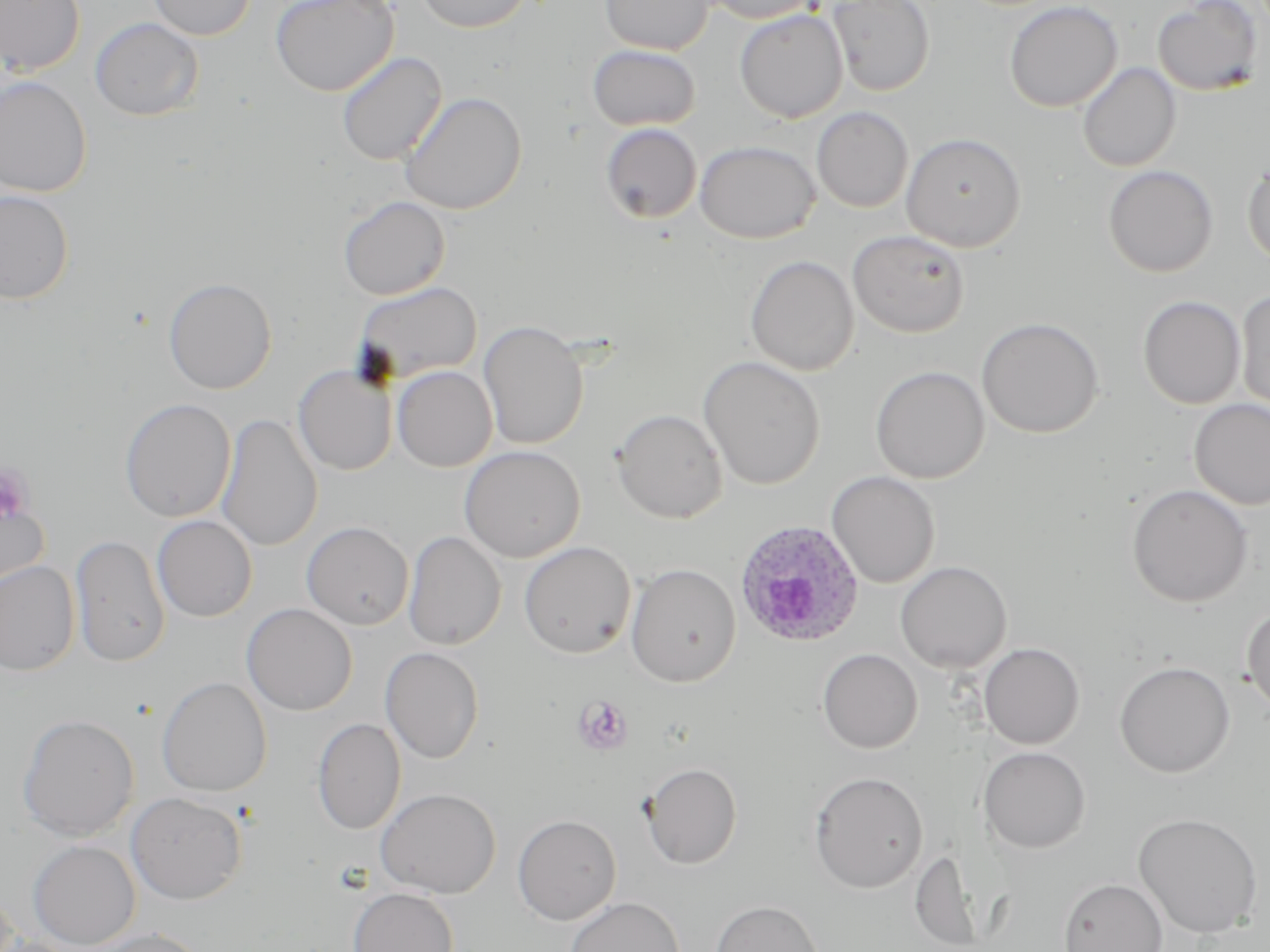

slide_level_diagnosis: Plasmodium ovale
magnification: 1000x
plasmodium_ovale_infected_red_blood_cell_locations: 'approximate bounding boxes as [x1, y1, x2, y2] in pixels: [735, 520, 864, 647]'
field_of_view: single
image_size: 1270×952 pixels
modality: optical microscopy
stain: May-Grünwald-Giemsa
preparation: thin blood film
platelet_locations: 'approximate bounding boxes as [x1, y1, x2, y2] in pixels: [0, 462, 35, 525], [573, 695, 634, 755]'
uninfected_red_blood_cell_locations: 'approximate bounding boxes as [x1, y1, x2, y2] in pixels: [0, 0, 85, 76], [147, 0, 255, 40], [270, 0, 399, 96], [415, 0, 533, 33], [599, 0, 713, 55], [697, 0, 822, 24], [827, 0, 935, 96], [1004, 0, 1123, 113], [1153, 0, 1264, 96], [734, 9, 848, 123], [90, 17, 204, 121], [587, 45, 701, 131], [337, 51, 447, 166], [1077, 62, 1181, 173], [0, 76, 92, 197], [400, 91, 526, 215], [812, 107, 914, 213], [600, 123, 702, 223], [901, 132, 1027, 252], [695, 140, 820, 243], [1243, 159, 1270, 267], [1103, 165, 1218, 277], [0, 190, 74, 305], [338, 196, 450, 300], [848, 230, 970, 338], [745, 255, 859, 376], [163, 277, 277, 394], [354, 282, 482, 384], [1235, 290, 1270, 415], [1138, 296, 1246, 409], [976, 317, 1104, 438], [479, 319, 589, 450], [698, 356, 825, 491], [293, 364, 397, 475], [392, 365, 497, 472], [871, 366, 989, 483], [119, 398, 236, 522], [1188, 398, 1270, 510], [611, 408, 728, 523], [215, 413, 323, 551], [460, 445, 585, 562], [826, 471, 941, 588], [1126, 484, 1254, 607], [0, 491, 50, 598], [152, 515, 257, 622], [301, 521, 414, 630], [403, 531, 506, 650], [70, 534, 170, 667], [519, 541, 636, 658], [0, 561, 81, 676], [894, 561, 1012, 673], [626, 563, 741, 687], [241, 603, 358, 715], [1242, 605, 1270, 716], [978, 642, 1085, 749], [380, 646, 485, 764], [817, 648, 923, 753], [1114, 661, 1235, 777], [156, 676, 272, 797], [17, 714, 140, 842], [312, 718, 406, 834], [977, 746, 1091, 854], [641, 762, 742, 869], [809, 770, 929, 893], [376, 787, 501, 898], [126, 792, 247, 904], [1133, 812, 1264, 939], [513, 814, 621, 925], [28, 840, 140, 949], [1059, 878, 1168, 952], [348, 887, 458, 952], [566, 897, 684, 952], [710, 900, 823, 952], [91, 928, 211, 952], [0, 936, 81, 952]'